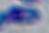

{
  "modality": "photomicrograph",
  "identification": "Toxoplasma gondii",
  "magnification": "1000x"
}